Describe the morphology of the erythrocytes.
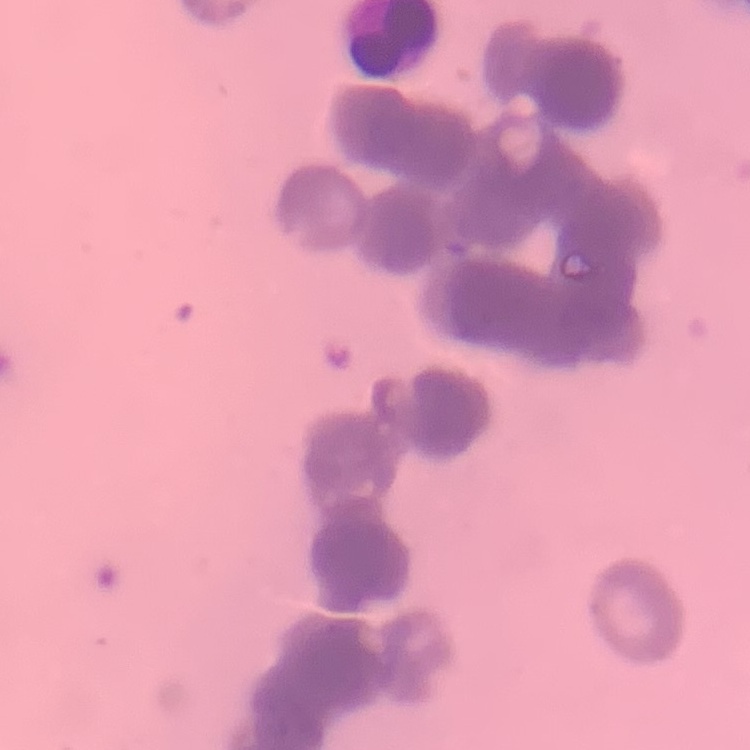
Rouleaux formation.

Summary:
  - Image type: one tile cut from a larger photomicrograph
  - Preparation: thin blood film
  - Stain: Field's or Giemsa